Classify this cell by malaria status.
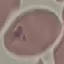
It is parasitized.

Summary:
  - Preparation: thin blood film
  - Stain: Giemsa
  - Capture: smartphone through the microscope eyepiece
  - Image type: automatically extracted cell patch, resized to 64 × 64 pixels